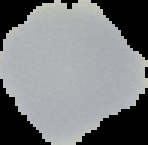

Summary:
  - Image size: 148×145 pixels
  - Preparation: thin blood smear
  - Image type: cell region segmented out of the field of view; surrounding area masked to black
  - Result: negative for malaria parasites